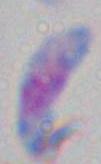

{
  "magnification": "1000x",
  "modality": "photomicrograph",
  "identification": "Toxoplasma gondii"
}